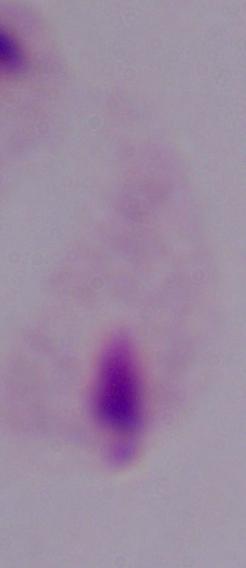

modality = photomicrograph
magnification = 1000x
identification = trichomonad